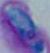 Toxoplasma gondii is shown. 1000x magnification. Micrograph.